Assess this cell for malaria.
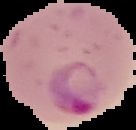
It is parasitized.

Summary:
  - Preparation: thin blood film
  - Image type: cell region segmented out of the field of view; surrounding area masked to black
  - Image size: 136×130 pixels